Classify this cell by malaria status.
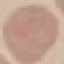

Uninfected.

Summary:
  - Image type: automatically extracted cell patch, resized to 64 × 64 pixels
  - Stain: Giemsa
  - Preparation: thin blood film
  - Capture: smartphone camera at the microscope eyepiece